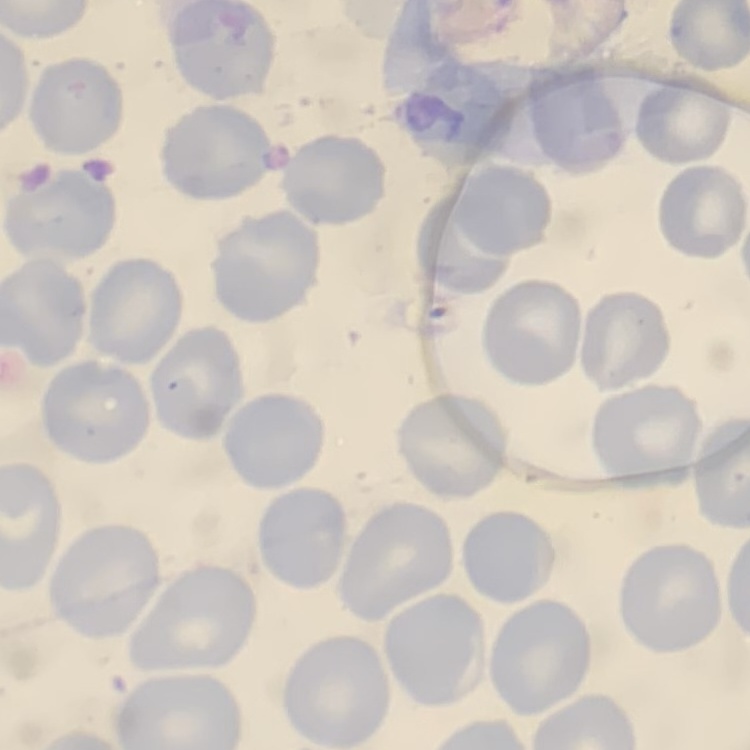

red blood cell morphology = no rouleaux formation
image type = one tile cut from a larger photomicrograph
stain = Field's or Giemsa
preparation = thin peripheral smear